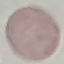 Result: no malaria parasites seen. Giemsa-stained preparation. Photographed with a smartphone camera at the microscope eyepiece. Thin blood film. Automatically extracted cell patch, resized to 64 × 64 pixels.